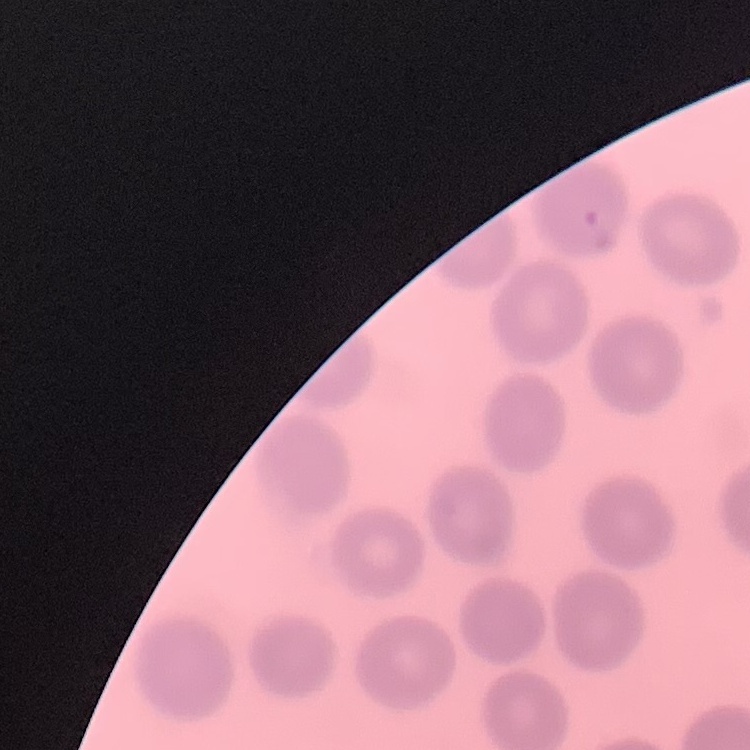 The erythrocytes show no rouleaux formation. Square crop of a larger photomicrograph. Field's or Giemsa stain. Thin peripheral smear.